Point out each leukocyte.
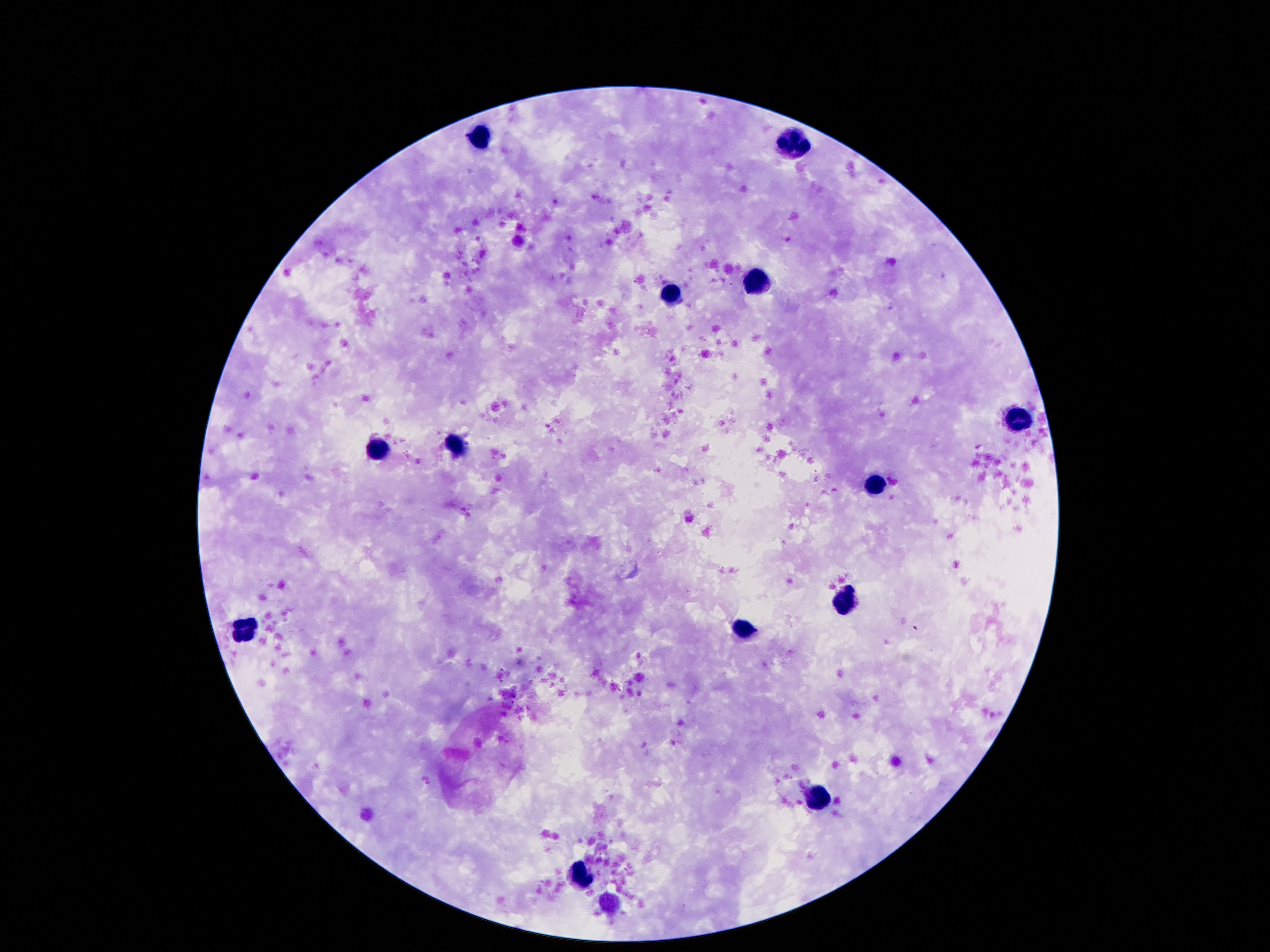
Approximate centers as [x, y] in pixels.
Leukocytes: [473, 136], [790, 143], [755, 281], [671, 294], [1011, 418], [456, 449], [375, 451], [877, 483], [845, 598], [746, 630], [242, 632], [818, 798], [583, 878].

Summary:
  - Preparation: thick peripheral-blood smear
  - Capture: smartphone camera through the microscope eyepiece
  - Image size: 1270×952 pixels
  - Magnification: 100x
  - Stain: Giemsa
  - Field of view: single
  - Patient malaria status: not infected